Give the extent of all uninfected red blood cells.
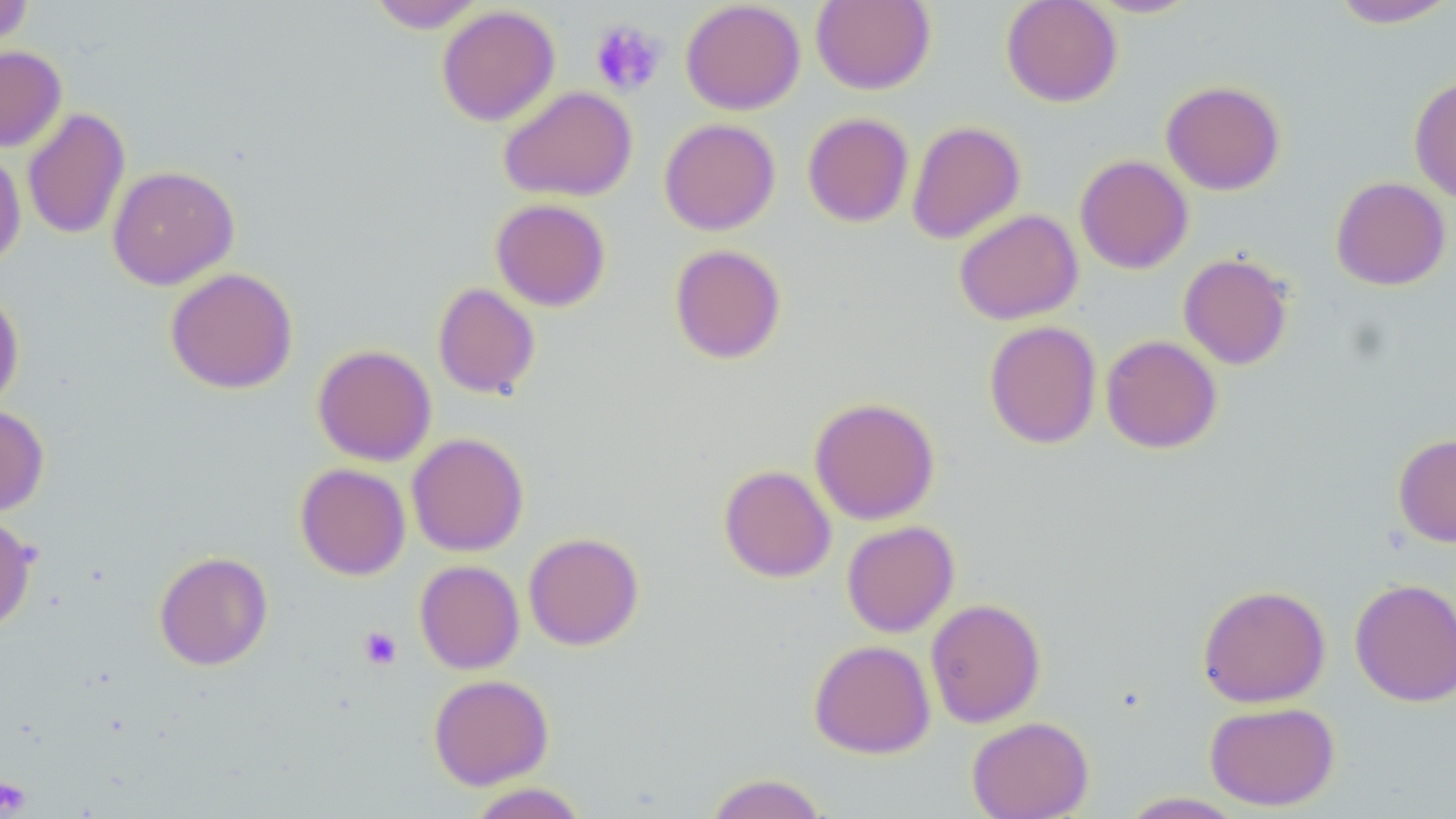
Approximate bounding boxes as [x1, y1, x2, y2] in pixels.
Uninfected red blood cells: [0, 0, 34, 53], [680, 0, 805, 115], [812, 0, 935, 94], [1001, 0, 1122, 107], [1086, 0, 1201, 18], [1328, 0, 1455, 29], [368, 1, 487, 33], [436, 5, 560, 126], [0, 45, 66, 152], [1409, 75, 1456, 203], [1161, 80, 1286, 195], [498, 86, 638, 202], [22, 107, 130, 240], [802, 112, 914, 228], [659, 118, 781, 235], [906, 120, 1026, 244], [0, 148, 26, 269], [1074, 154, 1193, 274], [107, 165, 239, 290], [1330, 176, 1451, 290], [490, 198, 611, 311], [954, 209, 1083, 325], [669, 244, 787, 364], [1178, 253, 1294, 370], [165, 267, 298, 394], [432, 282, 541, 399], [0, 286, 24, 412], [984, 320, 1102, 449], [1100, 335, 1222, 454], [312, 344, 436, 466], [809, 396, 940, 525], [0, 404, 49, 516], [407, 432, 529, 556], [1393, 433, 1456, 547], [295, 463, 410, 580], [718, 464, 836, 582], [0, 513, 37, 635], [841, 520, 960, 637], [523, 532, 644, 650], [154, 551, 273, 670], [415, 560, 524, 674], [1350, 577, 1456, 707], [1197, 584, 1331, 708], [925, 597, 1046, 728], [808, 639, 935, 758], [428, 674, 553, 789], [1204, 701, 1340, 811], [967, 716, 1094, 819], [704, 773, 830, 819], [466, 783, 589, 819], [1119, 792, 1247, 818].

Summary:
  - Platelet locations: [590, 20, 666, 96], [359, 626, 402, 669], [0, 778, 30, 815]
  - Slide-level diagnosis: negative for blood parasites
  - Preparation: thin blood film
  - Stain: May-Grünwald-Giemsa
  - Magnification: 1000x
  - Image size: 1456×819 pixels
  - Field of view: one of a larger specimen
  - Modality: light microscopy